Assess this cell for malaria.
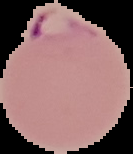

Parasitized.

Image is 133×154 pixels. Segmented cell region on a black background. From a thin blood smear.